Look for Plasmodium parasites.
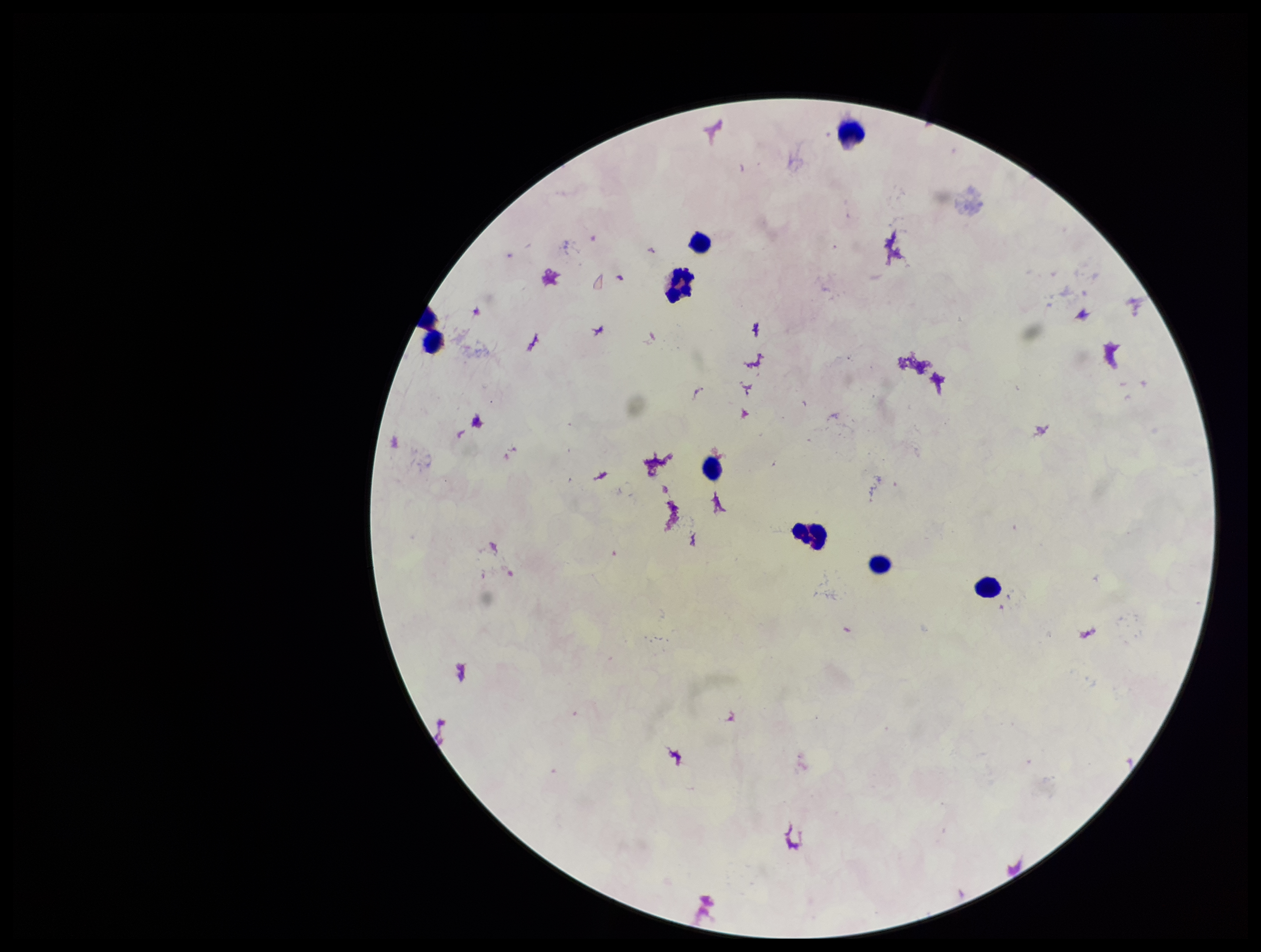
None identified.

Patient malaria status: negative. Image is 1261×952 pixels. Single field of view. Leukocyte count: 9. Preparation: thick blood smear. Stained with Giemsa. Smartphone photograph taken through the eyepiece of a microscope. Parasite count: 0.